Assess this cell for malaria.
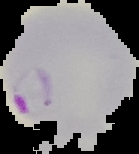

It is parasitized.

Image is 139×154 pixels. From a thin blood smear. Cell region segmented out of the field of view; the surrounding area is masked to black.